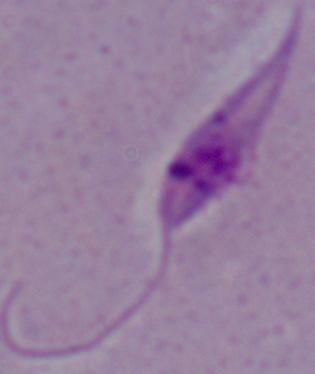

Captured at 1000x magnification. Micrograph. A Leishmania parasite is seen.